State which parasite is depicted.
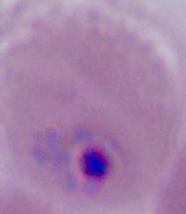
Plasmodium.

Summary:
  - Modality: micrograph
  - Magnification: 400x or 1000x